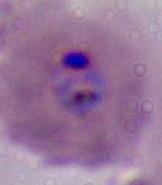
magnification = 400x or 1000x
modality = micrograph
identification = Plasmodium